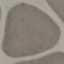

Malaria status: uninfected. Thin blood smear. Acquired by smartphone through the microscope eyepiece. Giemsa stain. Cell patch, automatically extracted from a larger field of view and resized to 64 × 64 pixels.